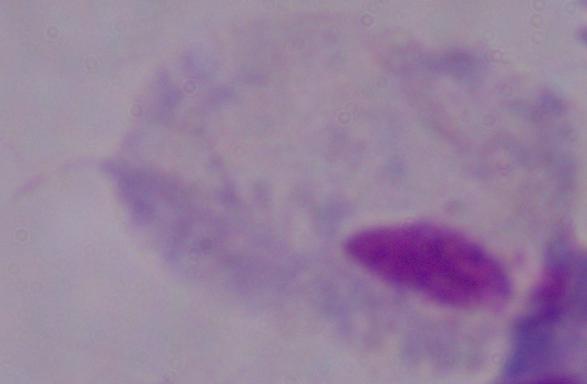

magnification = 1000x
modality = photomicrograph
identification = trichomonad